Outline platelets.
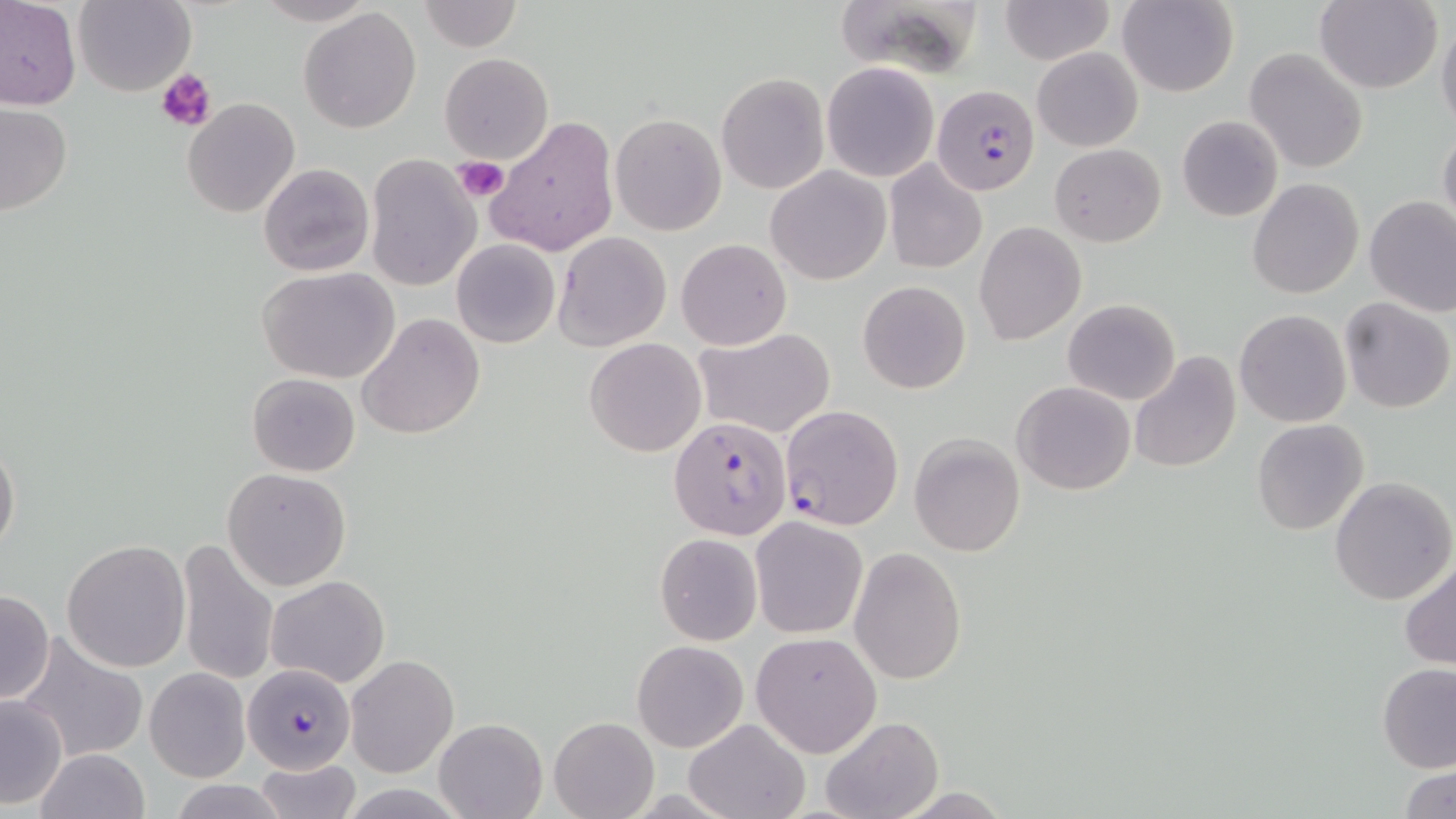

Approximate bounding boxes as [x1, y1, x2, y2] in pixels.
Platelets: [156, 67, 217, 132], [455, 156, 508, 200].

Uninfected red blood cell locations: [0, 0, 82, 109], [73, 0, 196, 97], [249, 0, 380, 26], [997, 0, 1114, 64], [1117, 0, 1237, 97], [420, 1, 522, 52], [834, 1, 991, 75], [1314, 1, 1442, 93], [297, 6, 421, 134], [1437, 16, 1456, 137], [1033, 47, 1143, 151], [1245, 47, 1367, 175], [439, 52, 553, 165], [822, 62, 940, 182], [716, 73, 830, 193], [182, 98, 300, 218], [0, 102, 73, 215], [609, 112, 726, 236], [487, 115, 619, 257], [1177, 115, 1283, 221], [1438, 123, 1456, 236], [1051, 143, 1165, 247], [364, 153, 483, 292], [883, 159, 987, 273], [258, 162, 374, 277], [766, 165, 891, 284], [1248, 178, 1364, 298], [1244, 182, 1358, 425], [1364, 194, 1456, 316], [973, 222, 1087, 347], [554, 231, 671, 350], [677, 238, 791, 350], [450, 239, 560, 349], [257, 266, 402, 385], [857, 280, 972, 393], [1338, 298, 1455, 415], [1062, 299, 1181, 405], [1234, 310, 1353, 428], [358, 313, 485, 440], [693, 329, 837, 440], [585, 337, 707, 456], [1128, 351, 1241, 474], [247, 373, 361, 476], [1012, 382, 1136, 495], [1250, 418, 1370, 536], [909, 433, 1026, 556], [1, 434, 20, 561], [221, 467, 352, 591], [1329, 477, 1456, 606], [750, 516, 868, 640], [654, 534, 762, 645], [61, 538, 191, 671], [175, 540, 279, 689], [848, 547, 967, 686], [1400, 558, 1456, 670], [266, 574, 389, 688], [0, 589, 55, 704], [750, 631, 883, 758], [14, 632, 150, 766], [631, 640, 748, 752], [345, 654, 460, 778], [1378, 661, 1456, 773], [144, 668, 251, 782], [0, 695, 69, 810], [819, 715, 944, 819], [550, 716, 659, 819], [684, 717, 808, 819], [434, 718, 547, 819], [35, 748, 149, 819], [252, 756, 360, 819], [1400, 765, 1454, 819], [169, 780, 292, 818]. Plasmodium falciparum-infected red blood cell locations: [931, 84, 1039, 195], [779, 404, 904, 531], [669, 414, 793, 540], [243, 664, 355, 773]. Slide-level diagnosis: Plasmodium falciparum. Light microscopy. Image is 1456×819 pixels. 1000x magnification. May-Grünwald-Giemsa-stained preparation. Single field of view. Thin blood smear.